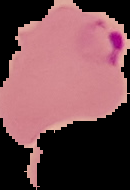
image_type: segmented cell region with the area outside set to black
malaria_status: parasitized
preparation: thin blood smear
image_size: 130×190 pixels